Identify the cell.
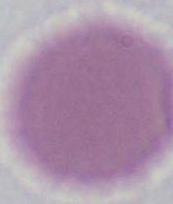
An erythrocyte.

1000x magnification. Micrograph.